Assess for parasitized red blood cells.
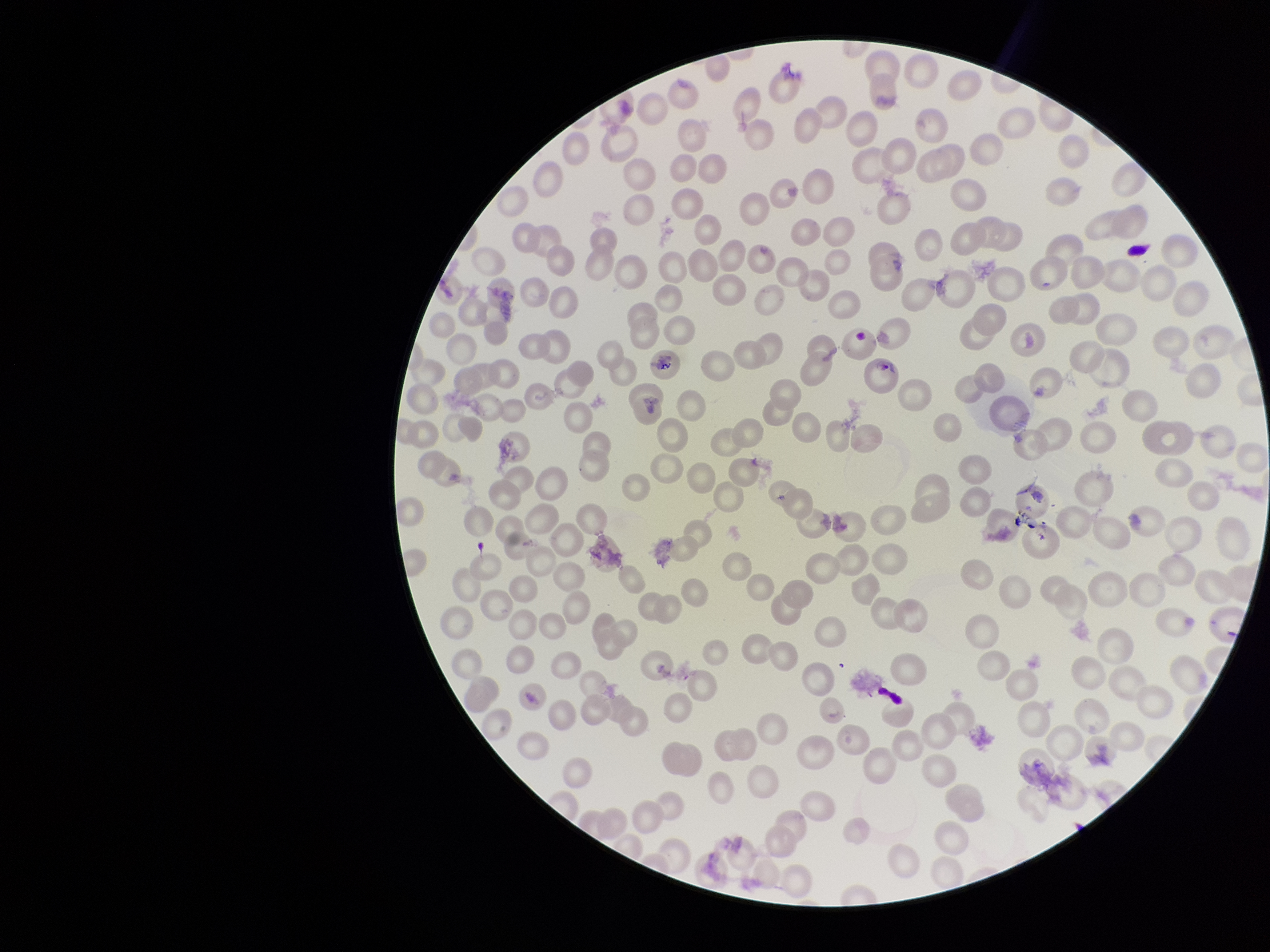
Identified.

Species reported for this patient: Plasmodium vivax. Preparation: thin smear. One field from this slide. Image is 1270×952 pixels. Red blood cell count: 215. Giemsa stain. Photographed through the microscope eyepiece with a smartphone camera. Patient malaria status: positive. Parasitized red blood cell count: 1.